Classify this cell by malaria status.
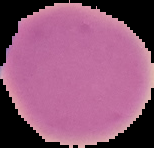
Uninfected.

{
  "image_size": "154×148 pixels",
  "preparation": "thin blood film",
  "image_type": "cell region segmented out of the field of view; surrounding area masked to black"
}